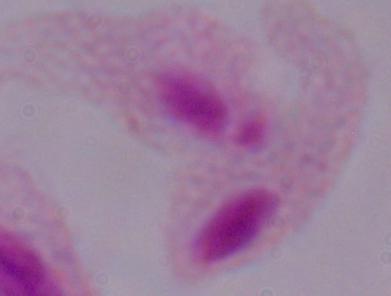
Summary:
  - Modality: micrograph
  - Identification: trichomonad
  - Magnification: 1000x